Report the malaria status of this cell.
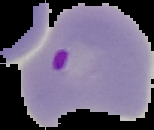

It is parasitized.

Summary:
  - Preparation: thin blood smear
  - Image size: 154×130 pixels
  - Image type: cell region segmented out of the field of view; surrounding area masked to black